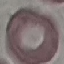
Summary:
  - Result: no malaria parasites detected
  - Stain: Giemsa
  - Image type: automatically extracted cell patch, resized to 64 × 64 pixels
  - Capture: smartphone through the microscope eyepiece
  - Preparation: thin blood smear